Look for Plasmodium parasites.
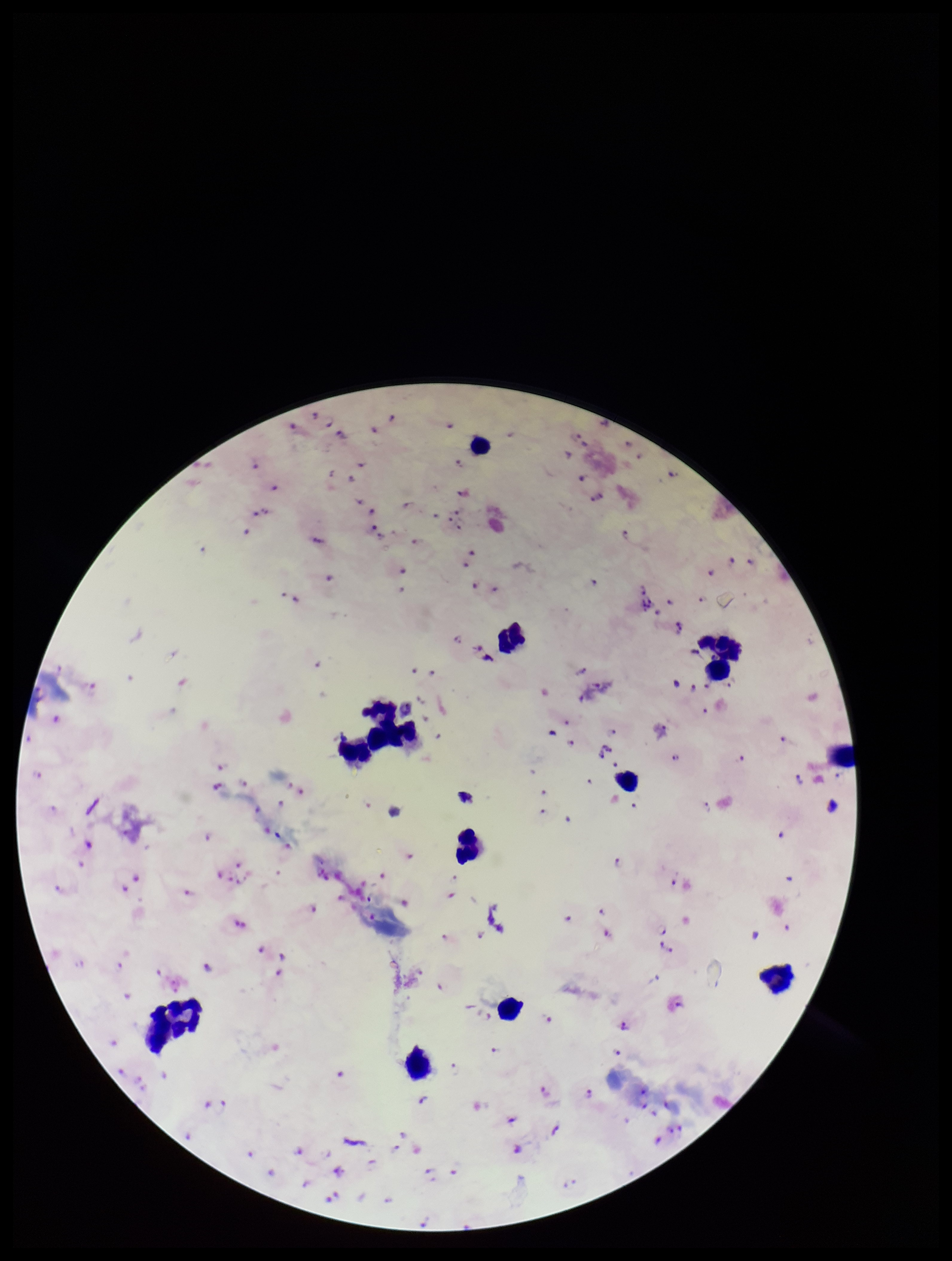

Identified.

Smartphone photograph taken through the eyepiece of a microscope. Image is 952×1261 pixels. Preparation: thick blood smear. Single field of view. Parasite count: 117. Species reported for this patient: Plasmodium falciparum. Patient malaria status: infected. Giemsa stain. Leukocyte count: 13.